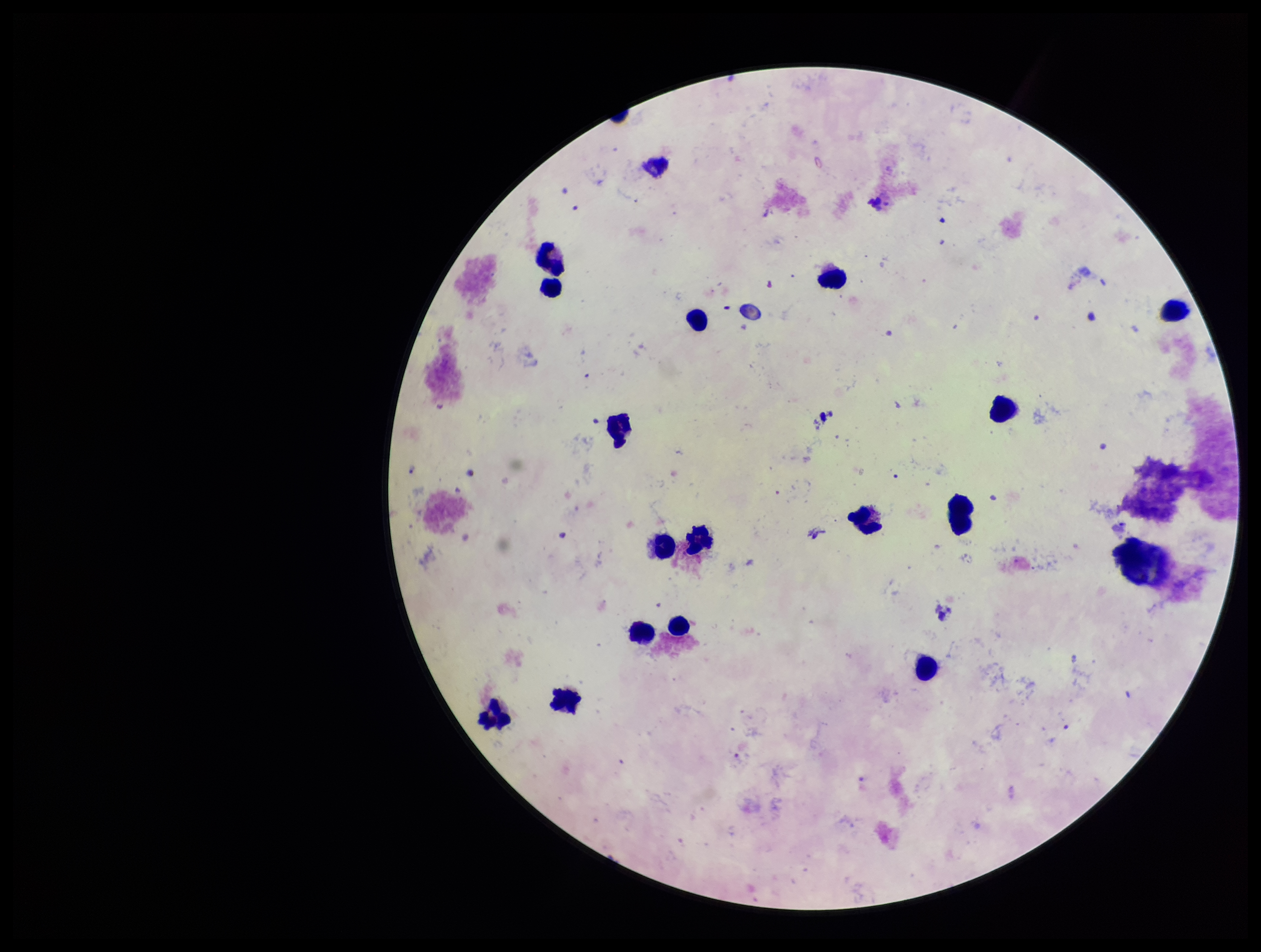

Summary:
  - Preparation: thick
  - Field of view: single
  - Plasmodium parasites: none seen
  - Leukocyte count: 17
  - Image size: 1261×952 pixels
  - Parasite count: 0
  - Patient malaria status: negative
  - Capture: smartphone photograph through the microscope eyepiece
  - Stain: Giemsa